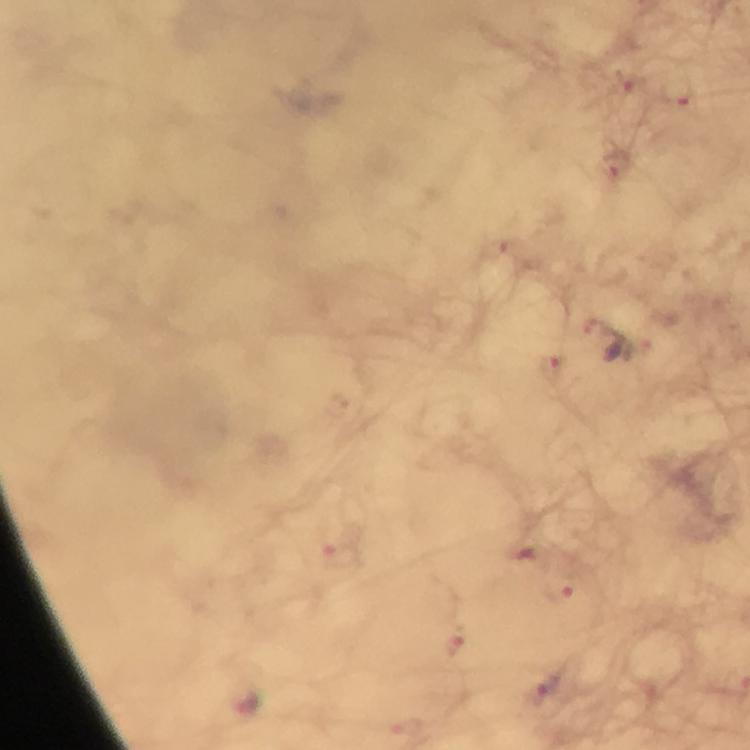 Approximate centers as [x, y] in pixels. Plasmodium parasite locations: [630, 81], [613, 164], [507, 245], [598, 322], [550, 367], [523, 551], [342, 558], [559, 592], [454, 645], [546, 690], [246, 703]. From a diagnostic examination for malaria. Smartphone photograph taken through a microscope. Image is 750×750 pixels. Immersion oil applied. A crop from one field of view. 100x magnification. Giemsa-stained preparation. Thick smear.